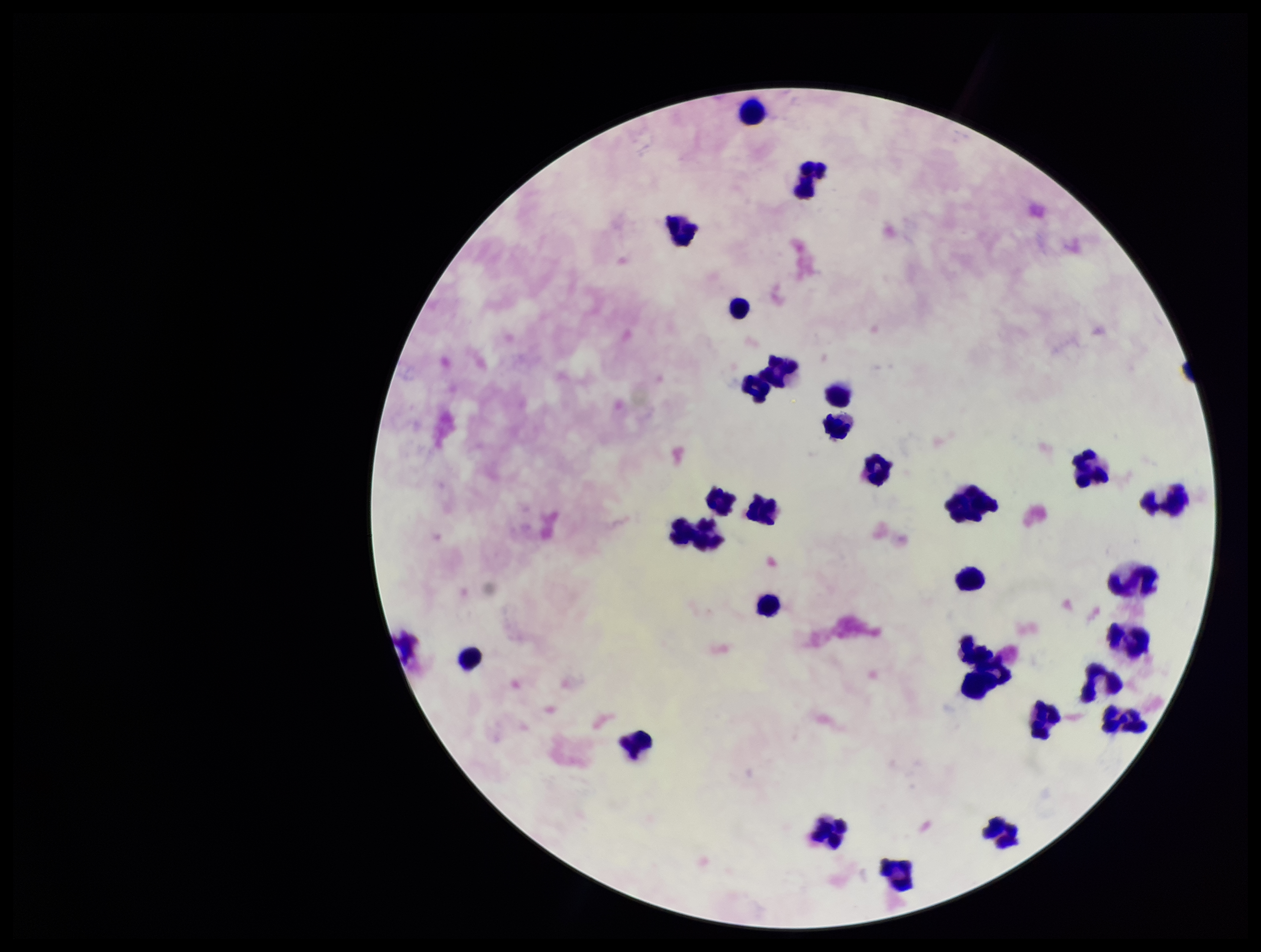

Summary:
  - Stain: Giemsa
  - Image size: 1261×952 pixels
  - Preparation: thick
  - Parasite count: 0
  - Capture: smartphone photograph through the microscope eyepiece
  - Patient malaria status: negative
  - Field of view: one from this slide
  - Leukocyte count: 30
  - Plasmodium parasites: none identified